Locate and identify every blood parasite.
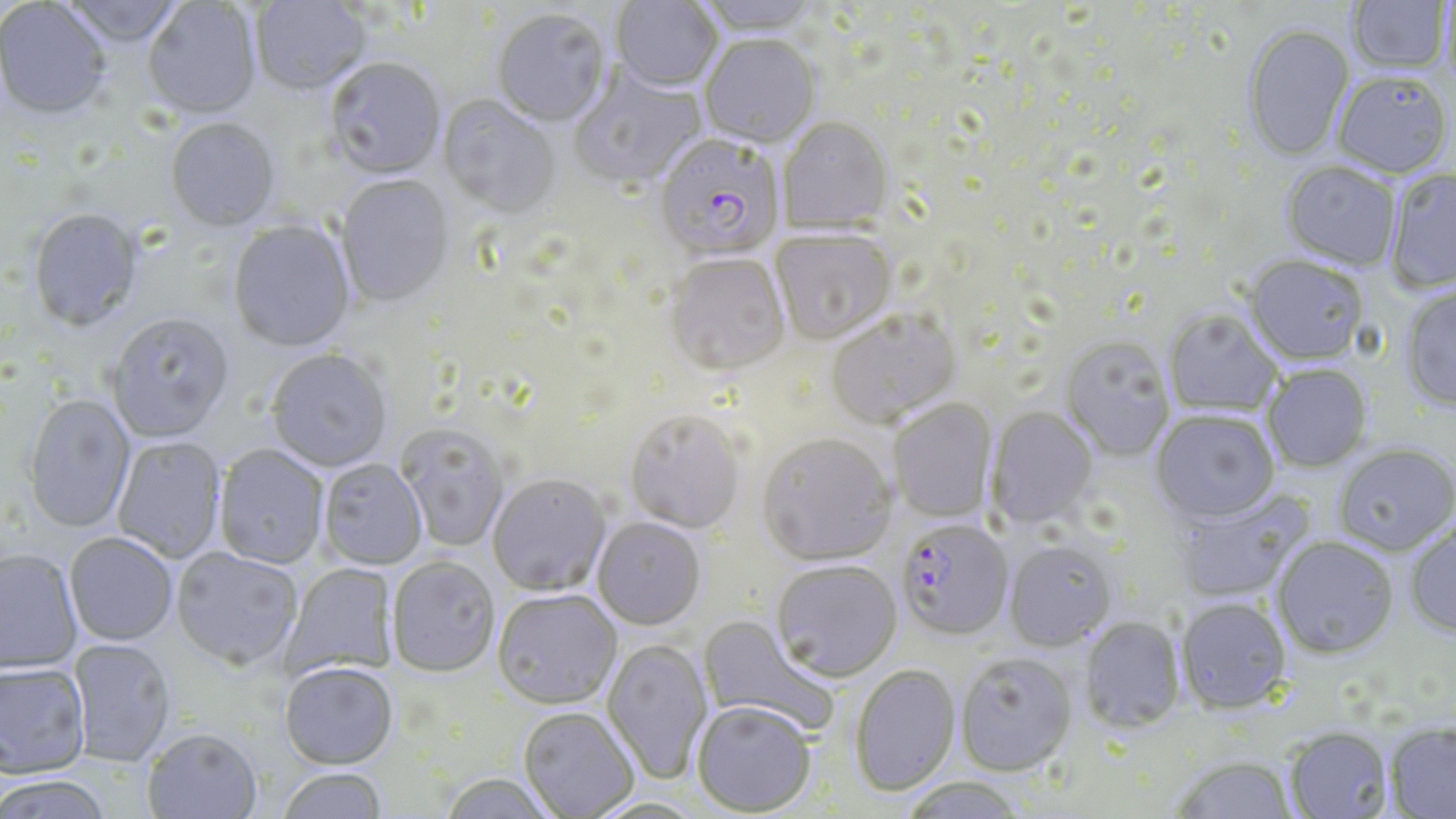

Approximate bounding boxes as (x1,y1)-(x2,y2) corner pairs in pixels.
Plasmodium falciparum-infected red blood cells: (658,137)-(778,263), (895,520)-(1014,642).
No Plasmodium ovale, Plasmodium malariae, Plasmodium vivax, Babesia divergens, or Trypanosoma brucei observed.

Uninfected red blood cell locations: (60,0)-(186,50), (251,0)-(371,97), (611,0)-(723,94), (693,0)-(824,38), (1347,0)-(1451,75), (1439,0)-(1456,99), (142,1)-(261,121), (0,2)-(111,123), (491,11)-(611,129), (1242,25)-(1354,164), (700,37)-(820,151), (324,59)-(446,182), (569,66)-(708,193), (1332,73)-(1452,179), (438,97)-(561,219), (778,118)-(894,234), (165,120)-(280,234), (1281,162)-(1402,272), (1385,169)-(1456,295), (334,176)-(455,310), (27,210)-(144,335), (227,220)-(356,354), (769,231)-(897,347), (663,255)-(791,380), (1243,256)-(1369,367), (1400,286)-(1456,413), (1163,309)-(1283,417), (826,311)-(963,429), (105,315)-(235,445), (1059,338)-(1175,463), (265,351)-(393,473), (1262,365)-(1373,472), (22,395)-(136,534), (888,399)-(997,523), (987,407)-(1099,528), (625,411)-(746,535), (1151,412)-(1279,524), (397,425)-(510,552), (757,436)-(897,568), (112,437)-(227,564), (213,445)-(329,571), (1334,446)-(1456,556), (318,460)-(427,571), (487,475)-(612,598), (1172,489)-(1312,602), (592,519)-(707,632), (1405,524)-(1456,640), (64,534)-(178,647), (1272,538)-(1399,660), (1004,540)-(1117,651), (171,548)-(302,672), (0,551)-(83,676), (386,558)-(501,679), (771,562)-(902,684), (279,564)-(400,681), (492,591)-(623,712), (1176,598)-(1292,715), (697,615)-(836,737), (1078,617)-(1184,733), (601,639)-(713,785), (67,640)-(177,768), (955,653)-(1078,776), (0,664)-(91,780), (278,664)-(398,772), (849,664)-(961,798), (692,702)-(817,816), (518,709)-(639,818), (1385,723)-(1456,817), (1285,727)-(1394,819), (142,729)-(263,819), (1170,755)-(1300,819), (277,769)-(388,819), (437,774)-(561,819), (0,777)-(114,819), (898,777)-(1029,819). Slide-level diagnosis: Plasmodium falciparum. 1000x magnification. May-Grünwald-Giemsa stain. Single field of view. Thin blood film. Image is 1456×819 pixels. Optical microscopy.